Name the cell type shown.
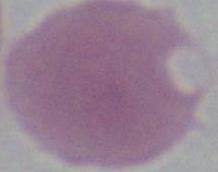

An erythrocyte.

Summary:
  - Magnification: 1000x
  - Modality: micrograph